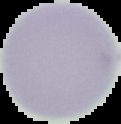
Image is 121×124 pixels. From a thin blood smear. Result: no Plasmodium parasites detected. The area outside the segmented cell region is set to black.